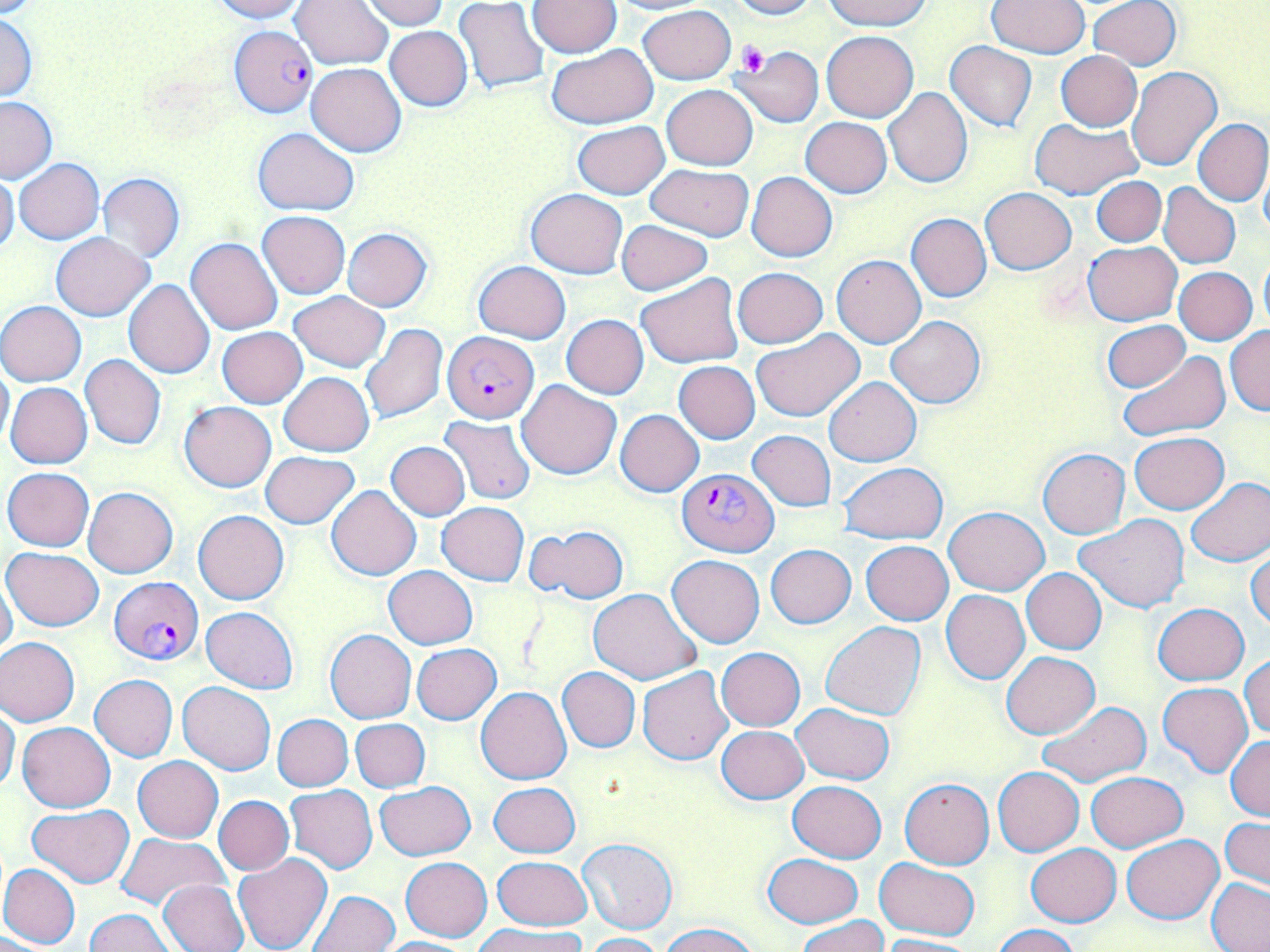

slide-level diagnosis = Plasmodium falciparum
image size = 1270×952 pixels
stain = May-Grünwald-Giemsa
preparation = thin blood smear
magnification = 1000x
Plasmodium falciparum-infected red blood cell locations = approximate bounding boxes as (x1, y1, x2, y2) in pixels: (229, 25, 318, 117), (443, 331, 537, 422), (677, 469, 777, 556), (108, 577, 203, 664)
uninfected red blood cell locations = approximate bounding boxes as (x1, y1, x2, y2) in pixels: (210, 0, 307, 22), (360, 0, 449, 30), (604, 0, 716, 14), (725, 0, 819, 19), (822, 0, 932, 30), (987, 0, 1089, 57), (1090, 0, 1181, 69), (291, 1, 394, 69), (528, 1, 621, 57), (455, 2, 550, 96), (638, 4, 735, 83), (0, 11, 37, 101), (385, 26, 472, 111), (821, 31, 918, 121), (946, 41, 1037, 132), (547, 45, 658, 128), (733, 46, 825, 128), (1057, 51, 1142, 131), (305, 62, 407, 156), (1127, 66, 1223, 171), (662, 84, 757, 170), (884, 87, 972, 188), (0, 97, 56, 182), (801, 117, 892, 197), (1028, 118, 1142, 199), (1193, 119, 1270, 206), (572, 120, 669, 198), (253, 128, 358, 214), (14, 158, 104, 245), (645, 163, 754, 240), (1259, 166, 1270, 244), (746, 171, 838, 262), (0, 173, 19, 256), (97, 173, 185, 262), (1092, 176, 1167, 246), (1090, 180, 1233, 255), (1158, 183, 1240, 269), (981, 187, 1076, 274), (526, 188, 628, 279), (257, 211, 350, 298), (906, 212, 991, 302), (615, 219, 715, 296), (341, 228, 431, 311), (52, 232, 154, 320), (186, 237, 283, 334), (1083, 241, 1181, 324), (831, 255, 925, 348), (1258, 255, 1270, 334), (474, 261, 571, 343), (1174, 267, 1257, 345), (733, 268, 828, 348), (635, 274, 744, 370), (124, 279, 215, 379), (289, 291, 389, 372), (0, 301, 86, 386), (562, 314, 649, 399), (885, 315, 985, 408), (1101, 320, 1191, 393), (360, 323, 448, 425), (1226, 326, 1270, 416), (217, 327, 308, 408), (751, 330, 864, 422), (1118, 351, 1229, 442), (79, 354, 166, 450), (0, 358, 12, 452), (674, 361, 760, 443), (279, 372, 374, 456), (823, 377, 921, 466), (517, 379, 621, 480), (5, 382, 92, 469), (179, 401, 277, 493), (616, 409, 704, 496), (441, 416, 535, 504), (748, 431, 836, 511), (1130, 432, 1228, 514), (386, 441, 469, 520), (1038, 448, 1130, 538), (260, 451, 360, 527), (839, 462, 947, 543), (3, 467, 94, 550), (1185, 477, 1270, 566), (326, 485, 422, 580), (84, 487, 177, 578), (438, 502, 527, 586), (943, 507, 1049, 594), (194, 509, 289, 605), (1075, 514, 1190, 612), (526, 525, 628, 604), (862, 541, 954, 625), (766, 544, 856, 628), (2, 547, 103, 631), (1246, 547, 1270, 631), (667, 555, 765, 648), (383, 566, 477, 649), (1021, 567, 1107, 654), (0, 570, 18, 662), (588, 588, 700, 685), (941, 590, 1030, 684), (1153, 603, 1248, 685), (202, 606, 299, 694), (820, 622, 926, 720), (324, 629, 416, 724), (0, 637, 81, 726), (412, 643, 502, 723), (716, 647, 806, 731), (1001, 651, 1100, 738), (1240, 654, 1270, 739), (638, 666, 734, 766), (557, 668, 640, 752), (89, 674, 178, 761), (178, 681, 275, 774), (1157, 683, 1252, 776), (476, 686, 572, 784), (1038, 701, 1151, 789), (793, 703, 894, 786), (0, 706, 20, 792), (272, 714, 353, 791), (351, 718, 430, 792), (18, 721, 115, 812), (717, 725, 808, 803), (1227, 736, 1270, 822), (134, 756, 223, 843), (993, 767, 1084, 856), (1086, 772, 1188, 852), (899, 776, 995, 869), (788, 781, 886, 863), (375, 782, 475, 860), (488, 782, 581, 858), (284, 785, 377, 874), (213, 796, 293, 876), (28, 804, 133, 888), (1220, 817, 1270, 891), (116, 833, 229, 910), (1120, 834, 1223, 923), (577, 838, 677, 934), (1026, 844, 1121, 925), (763, 852, 862, 928), (232, 853, 332, 952), (493, 855, 593, 930), (401, 857, 492, 941), (874, 857, 981, 940), (0, 863, 80, 950), (157, 879, 249, 952), (1206, 879, 1270, 951), (308, 890, 399, 952), (87, 909, 173, 952), (797, 915, 888, 952), (477, 922, 584, 952), (659, 923, 761, 952), (990, 925, 1080, 952), (0, 932, 59, 951), (579, 933, 666, 952), (877, 935, 979, 952), (375, 937, 472, 952)
modality = light microscopy
field of view = one of a larger specimen
platelet locations = approximate bounding boxes as (x1, y1, x2, y2) in pixels: (738, 41, 769, 75)